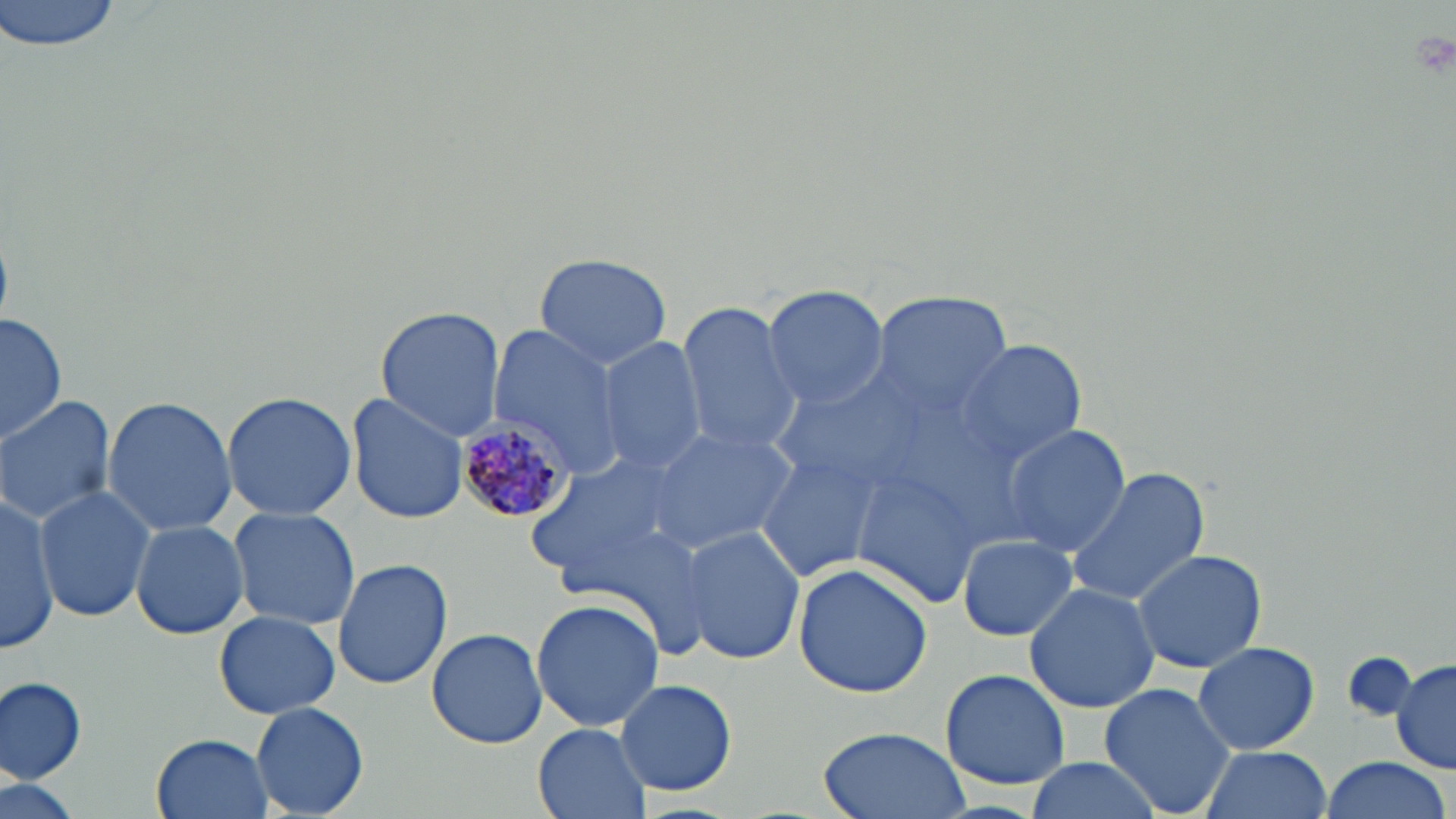

Summary:
  - Coordinate format: approximate bounding boxes as (x1, y1, x2, y2) in pixels
  - Plasmodium malariae-infected red blood cell locations: (452, 412, 574, 523)
  - Uninfected red blood cell locations: (0, 0, 126, 51), (534, 252, 674, 370), (763, 285, 888, 411), (873, 294, 1011, 417), (673, 298, 803, 455), (374, 306, 506, 439), (2, 313, 65, 450), (487, 325, 629, 481), (597, 336, 708, 475), (954, 337, 1088, 466), (222, 390, 356, 520), (347, 392, 470, 524), (0, 395, 117, 525), (104, 396, 236, 536), (646, 425, 798, 553), (1002, 425, 1130, 557), (752, 448, 883, 582), (522, 454, 688, 588), (1064, 464, 1210, 607), (34, 487, 155, 622), (0, 493, 58, 651), (228, 507, 362, 630), (130, 520, 251, 640), (680, 527, 806, 667), (959, 535, 1077, 640), (1132, 547, 1268, 674), (332, 558, 452, 689), (793, 565, 935, 700), (1025, 581, 1161, 714), (531, 598, 663, 732), (214, 612, 339, 718), (425, 627, 548, 751), (1193, 641, 1320, 754), (1341, 651, 1416, 723), (1391, 658, 1456, 775), (940, 668, 1071, 790), (0, 677, 88, 783), (616, 678, 736, 796), (1098, 681, 1238, 818), (251, 701, 370, 817), (531, 722, 653, 819), (817, 727, 968, 819), (152, 732, 274, 819), (1200, 744, 1332, 819), (1318, 756, 1451, 819), (1022, 757, 1166, 819), (2, 773, 86, 819)
  - Slide-level diagnosis: Plasmodium malariae
  - Modality: optical microscopy
  - Field of view: one of a larger specimen
  - Preparation: thin blood film
  - Magnification: 1000x
  - Stain: May-Grünwald-Giemsa
  - Image size: 1456×819 pixels